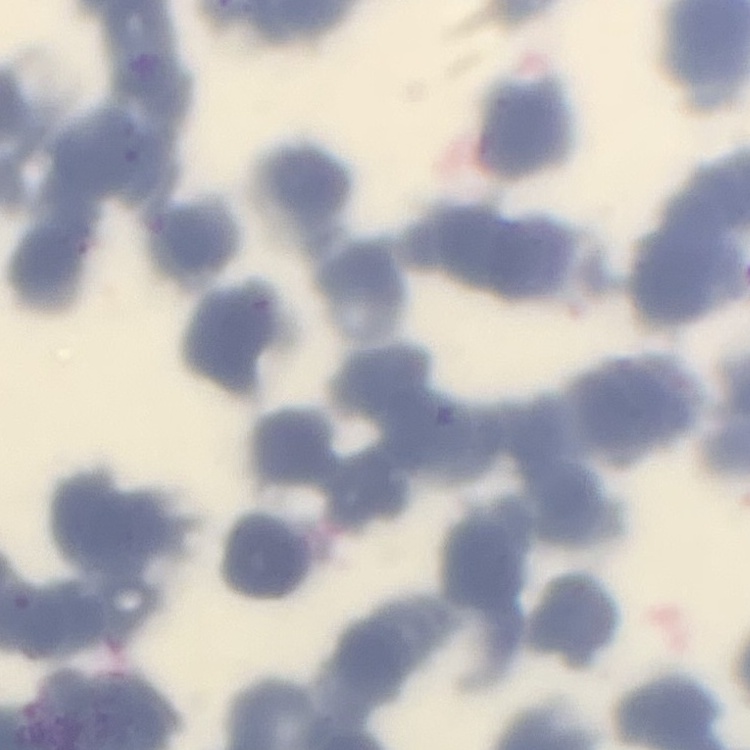

The erythrocytes show rouleaux formation. Square crop of a larger photomicrograph. Field's or Giemsa stain. Thin peripheral smear.